State the blood parasite species.
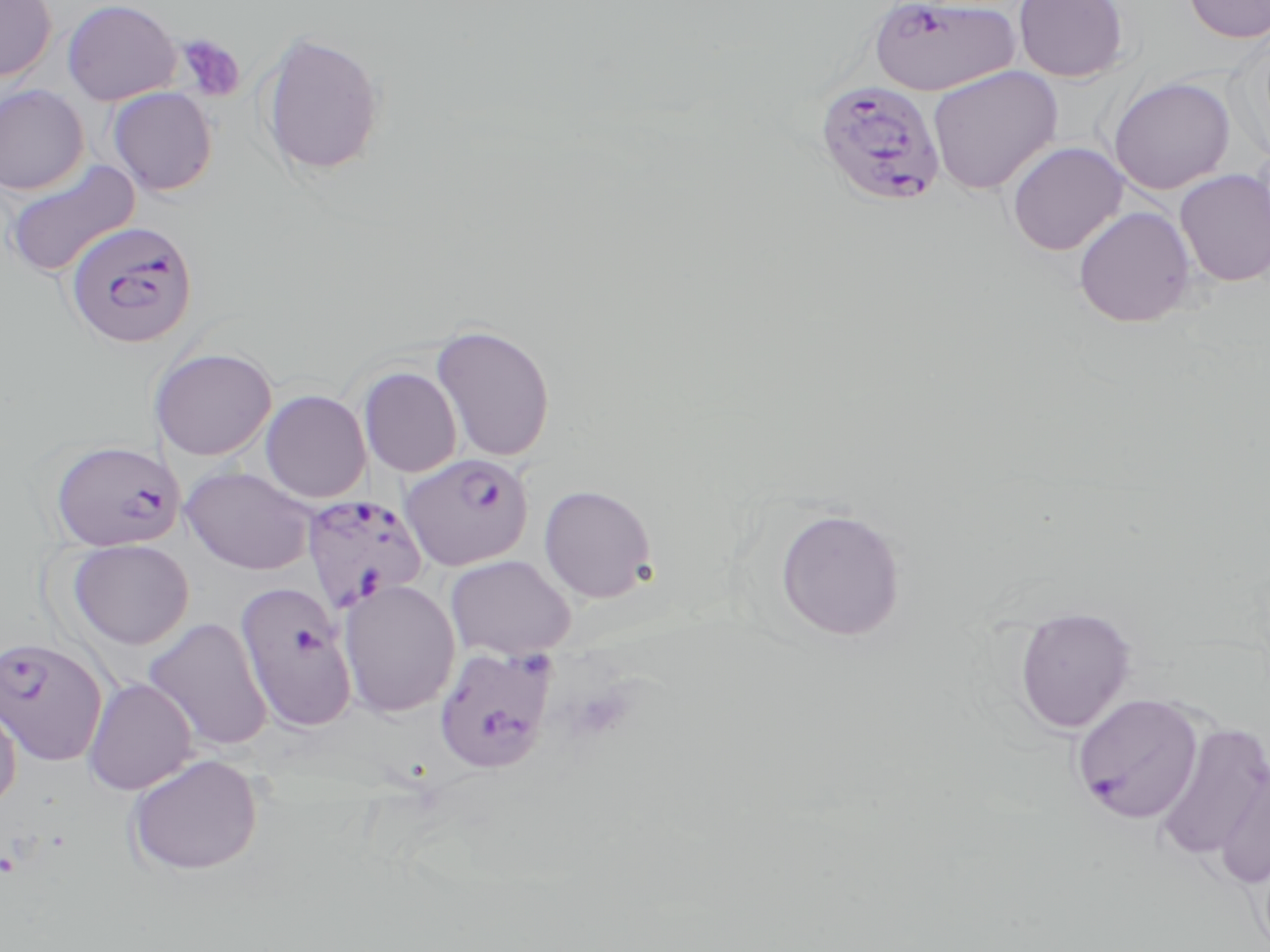
Plasmodium falciparum.

Approximate bounding boxes as (x1,y1)-(x2,y2) corner pairs in pixels. Plasmodium falciparum-infected red blood cell locations: (868,0)-(1020,97), (813,79)-(947,207), (62,219)-(198,350), (50,439)-(186,551), (399,453)-(534,571), (302,494)-(429,615), (234,582)-(358,733), (0,636)-(108,767), (433,646)-(558,774), (1071,693)-(1205,824). Platelet locations: (176,33)-(245,102). Uninfected red blood cell locations: (0,0)-(57,82), (1013,0)-(1129,82), (1181,0)-(1270,43), (61,1)-(180,105), (258,30)-(387,179), (927,65)-(1063,195), (1107,76)-(1236,194), (0,85)-(89,195), (107,87)-(218,196), (1007,141)-(1128,256), (4,160)-(140,279), (1174,169)-(1270,287), (1073,206)-(1197,328), (430,322)-(556,462), (149,346)-(277,461), (359,367)-(462,477), (260,390)-(371,503), (181,466)-(315,574), (538,484)-(657,604), (773,506)-(907,643), (66,539)-(194,650), (445,554)-(576,660), (340,579)-(461,717), (1013,606)-(1136,733), (143,617)-(272,752), (83,678)-(198,795), (0,692)-(21,814), (1152,722)-(1270,863), (125,753)-(264,876), (1214,762)-(1270,890). One field of a larger specimen. Thin blood film. Captured at 1000x magnification. Image is 1270×952 pixels. Light microscopy. May-Grünwald-Giemsa-stained preparation.